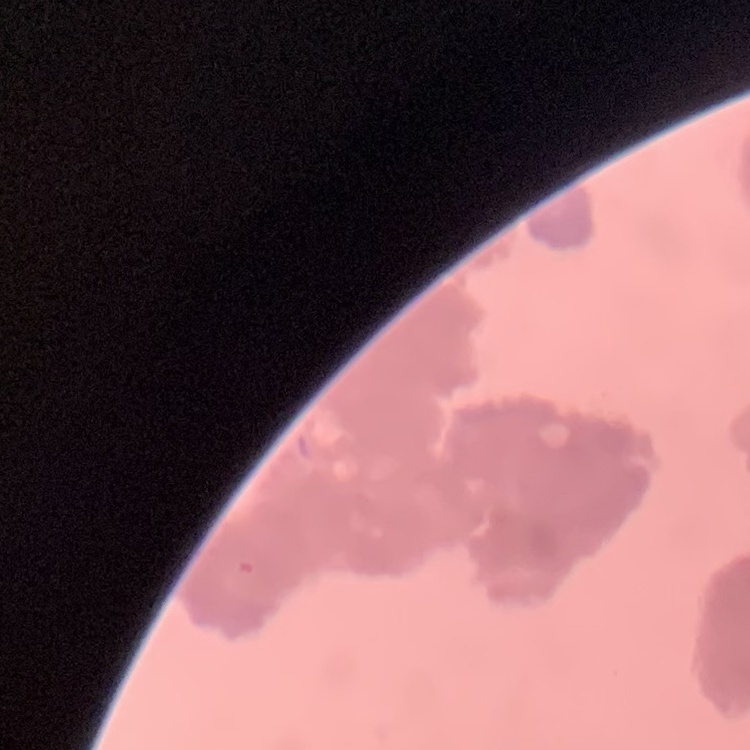
erythrocyte_morphology: rouleaux formation
stain: Field's or Giemsa
preparation: thin blood film
image_type: one tile cut from a larger photomicrograph